Report the malaria status of this cell.
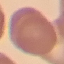

It is uninfected.

Thin blood film. Acquired by smartphone through the microscope eyepiece. Automatically extracted cell patch, resized to 64 × 64 pixels. Giemsa stain.